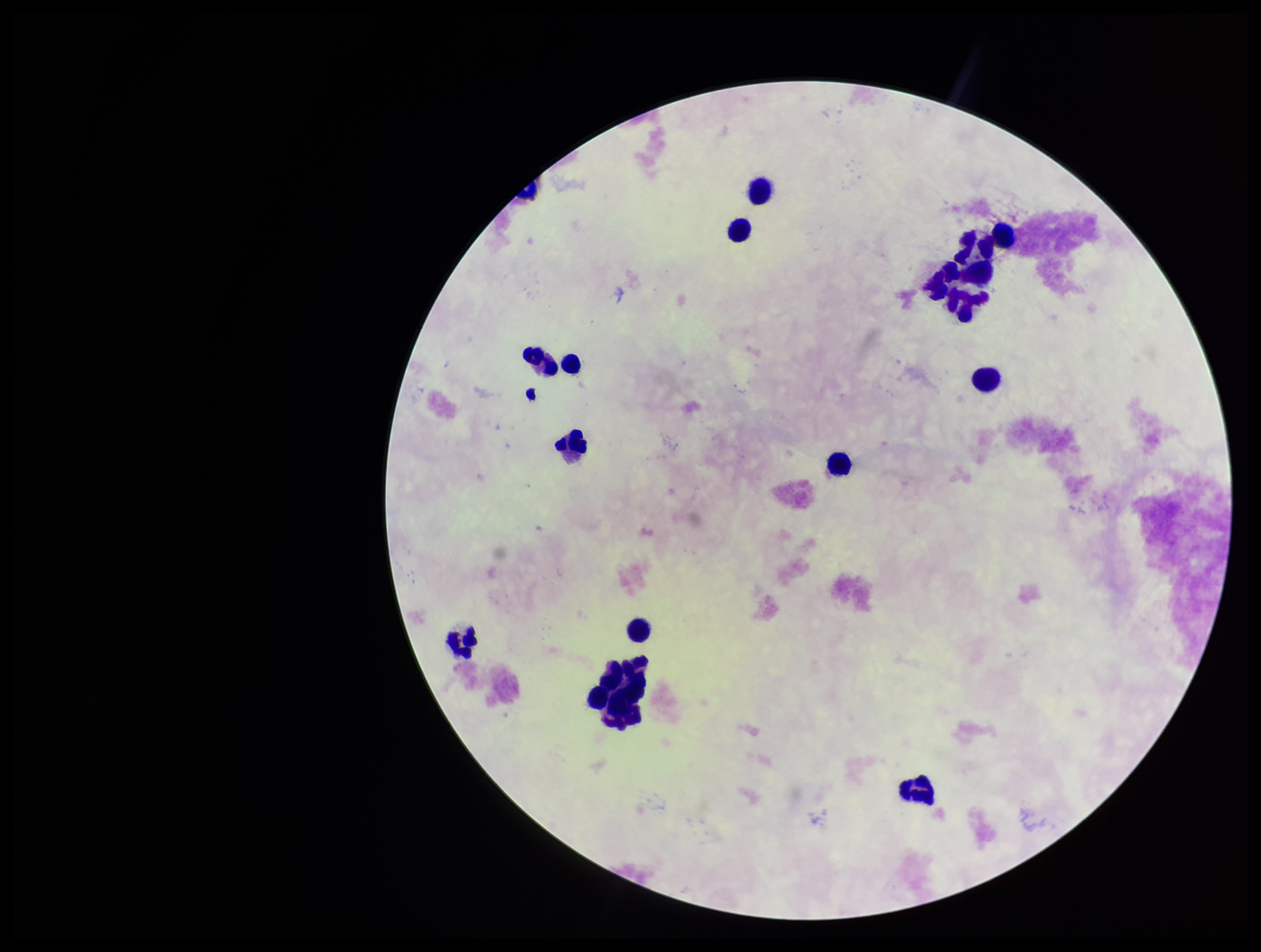

Summary:
  - Preparation: thick
  - Leukocyte count: 16
  - Field of view: one from this slide
  - Capture: smartphone photograph through the microscope eyepiece
  - Patient malaria status: negative
  - Image size: 1261×952 pixels
  - Stain: Giemsa
  - Parasite count: 0
  - Plasmodium parasites: none identified